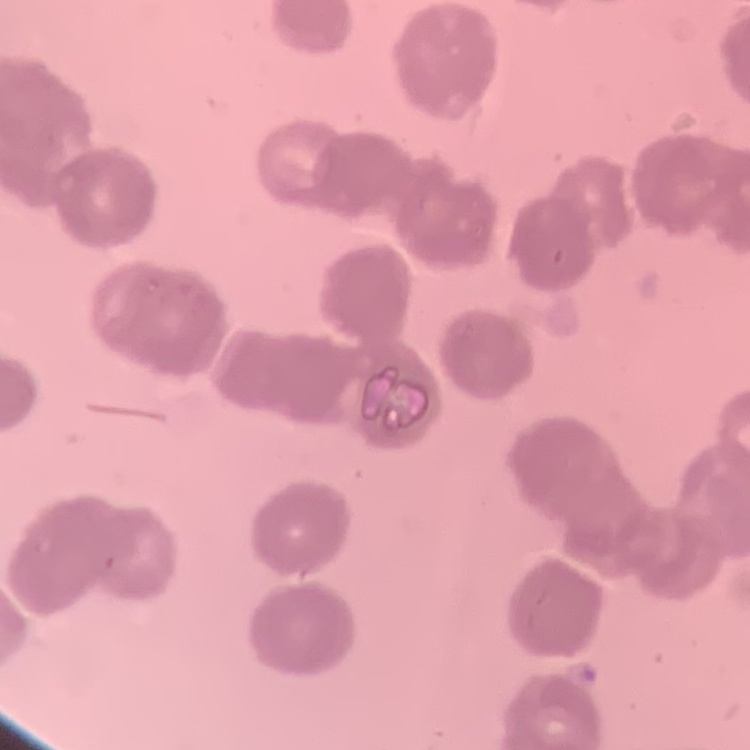
The red blood cells exhibit rouleaux formation. Field's or Giemsa stain. One tile cut from a larger photomicrograph. Thin blood film.